Locate every parasitized RBC.
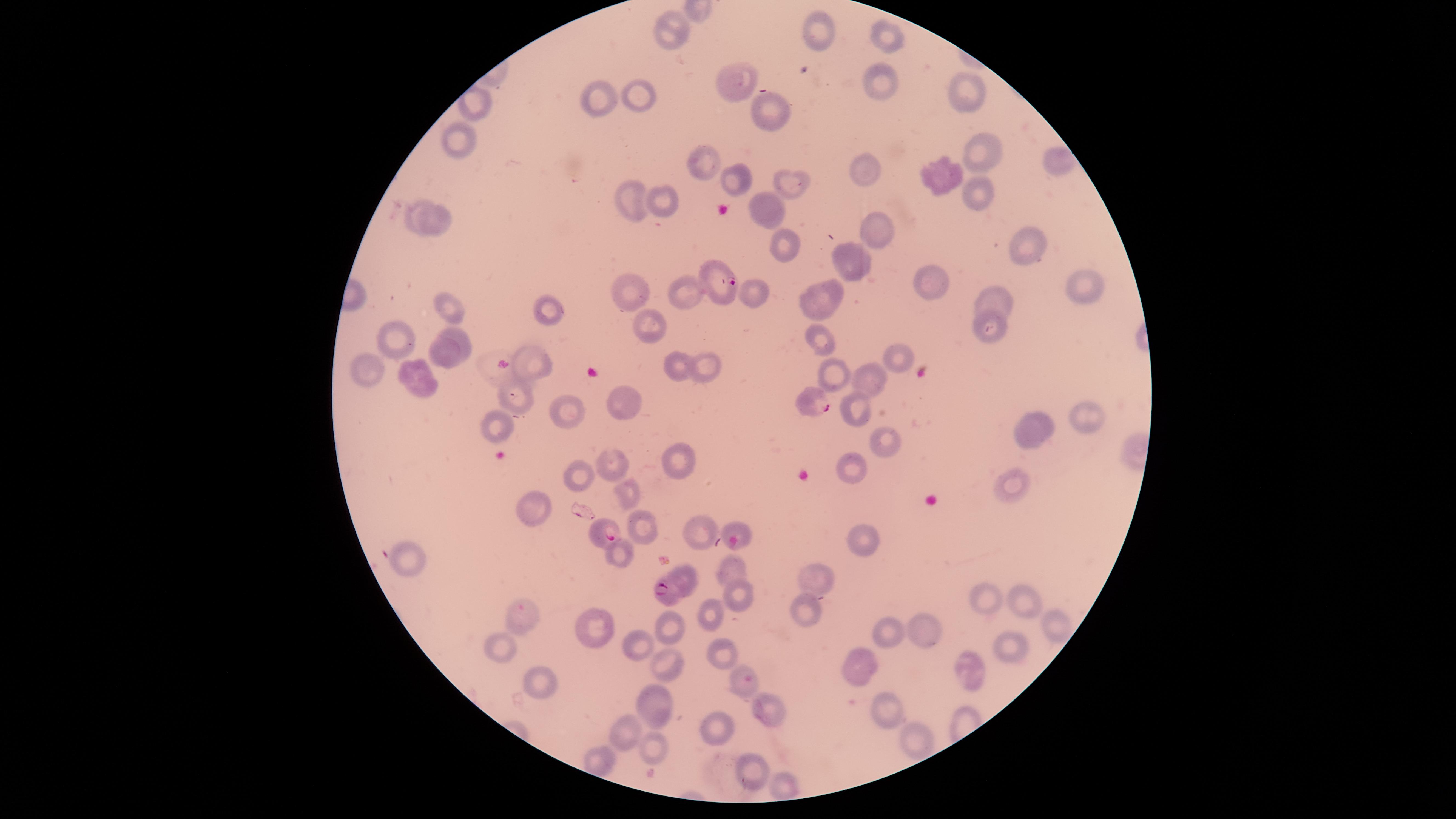
Approximate marker points as [x, y] in pixels.
Parasitized RBCs: [717, 277], [812, 404], [606, 533], [666, 593], [520, 616].

Approximate marker points as [x, y] in pixels. Uninfected RBCs: [819, 32], [675, 33], [884, 38], [732, 80], [882, 82], [969, 92], [638, 93], [598, 100], [473, 107], [771, 113], [458, 144], [977, 151], [1048, 159], [705, 162], [860, 167], [943, 176], [739, 180], [789, 182], [977, 193], [658, 196], [768, 203], [631, 204], [418, 208], [443, 219], [882, 231], [1026, 244], [786, 247], [851, 260], [923, 281], [635, 287], [1084, 287], [681, 293], [754, 293], [821, 299], [997, 301], [447, 306], [546, 311], [991, 316], [655, 325], [459, 335], [400, 338], [823, 343], [445, 355], [897, 359], [538, 362], [708, 365], [679, 368], [416, 369], [371, 371], [832, 371], [873, 379], [520, 398], [620, 401], [859, 405], [563, 408], [1084, 411], [490, 422], [1034, 429], [891, 444], [681, 459], [612, 461], [854, 465], [577, 473], [1016, 488], [625, 492], [530, 509], [700, 524], [737, 526], [643, 527], [867, 539], [412, 556], [621, 556], [730, 571], [682, 572], [818, 574], [735, 592], [987, 599], [1021, 599], [806, 601], [713, 610], [1053, 626], [594, 627], [671, 627], [928, 630], [892, 634], [1008, 644], [637, 645], [500, 649], [722, 651], [859, 664], [661, 665], [966, 671], [739, 679], [542, 681], [881, 703], [657, 705], [770, 708], [717, 727], [624, 734], [921, 737], [653, 748], [604, 763], [749, 767], [786, 789]. Image is 1456×819 pixels. Species: Plasmodium falciparum. Smartphone photograph through the microscope eyepiece. One field of view of the specimen. Circular visible region. Thin smear of blood. Giemsa stain.